Point out every Plasmodium parasite.
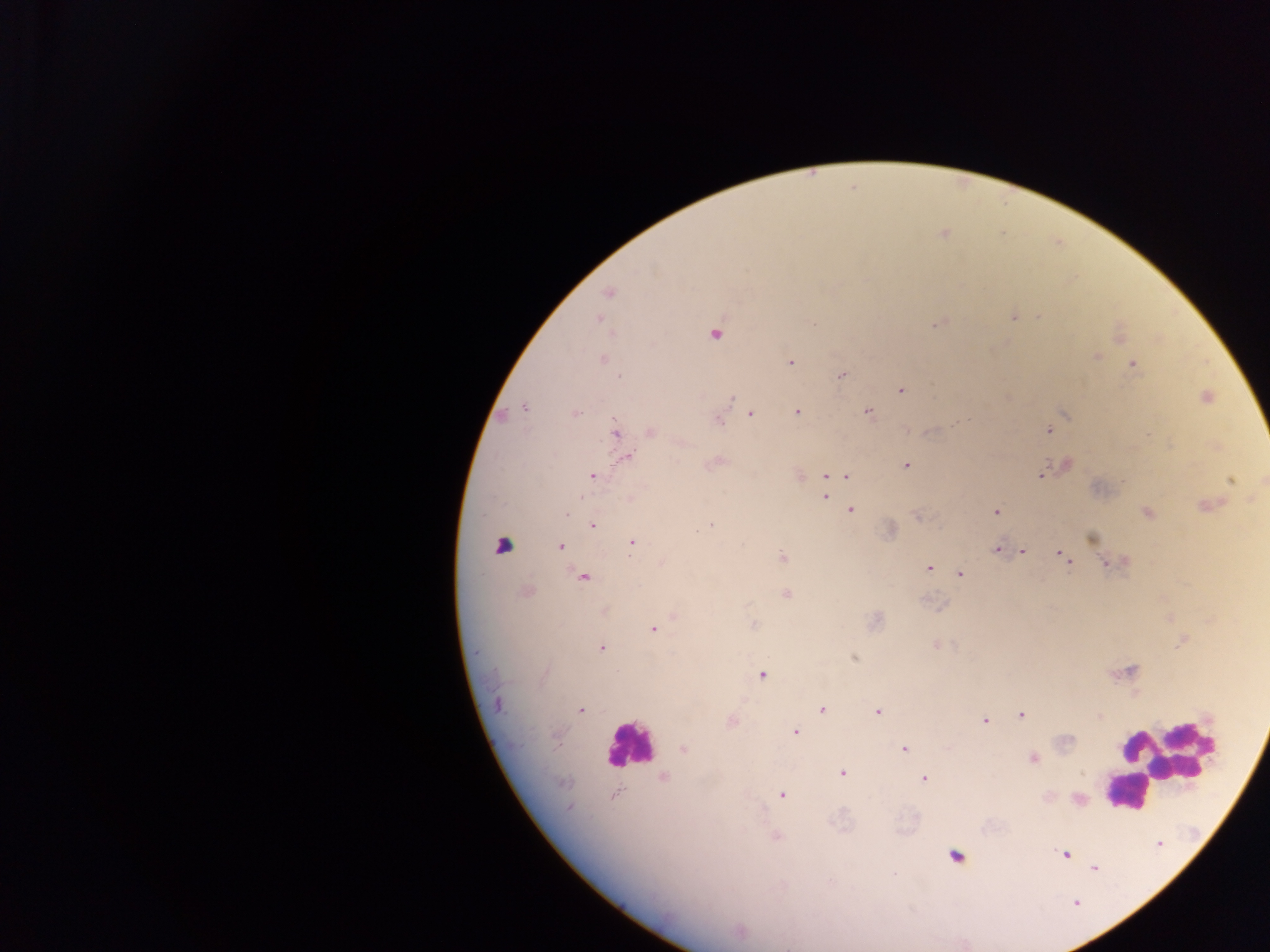
Approximate centers as x y in pixels.
Plasmodium parasites: 943 234; 608 292; 1039 315; 1013 316; 599 319; 938 323; 715 334; 1120 336; 1096 356; 602 358; 790 362; 1133 365; 841 375; 901 389; 1204 397; 732 398; 524 406; 868 411; 797 412; 1063 413; 574 414; 750 414; 718 419; 1049 429; 650 430; 614 432; 626 457; 715 462; 906 464; 1066 465; 1042 474; 797 475; 592 476; 825 476; 846 476; 1231 478; 825 496; 630 498; 1206 505; 850 509; 996 511; 565 512; 1147 512; 918 516; 592 525; 710 525; 889 530; 1091 538; 631 541; 560 547; 996 549; 1020 551; 1062 553; 782 557; 1067 560; 1122 561; 662 563; 1108 563; 928 567; 959 573; 582 576; 526 591; 786 593; 604 610; 673 616; 873 621; 754 625; 652 629; 1183 641; 935 645; 600 647; 853 657; 1128 671; 761 674; 496 703; 821 709; 579 710; 877 712; 1021 715; 1098 716; 984 720; 731 722; 795 732; 683 748; 903 749; 1032 757; 843 773; 663 777; 924 779; 782 794; 614 795; 1077 799; 569 807; 775 835; 1065 853; 1093 867; 739 931.
One object is labeled both Plasmodium parasite and leukocyte by the source: 502 544.

Summary:
  - Leukocyte locations: 629 745; 1163 761; 1140 779; 1123 797; 955 856
  - Field of view: single
  - Country: Ghana
  - Image size: 1270×952 pixels
  - Capture: mobile-phone photograph through a microscope
  - Preparation: thick blood smear